State the blood parasite species.
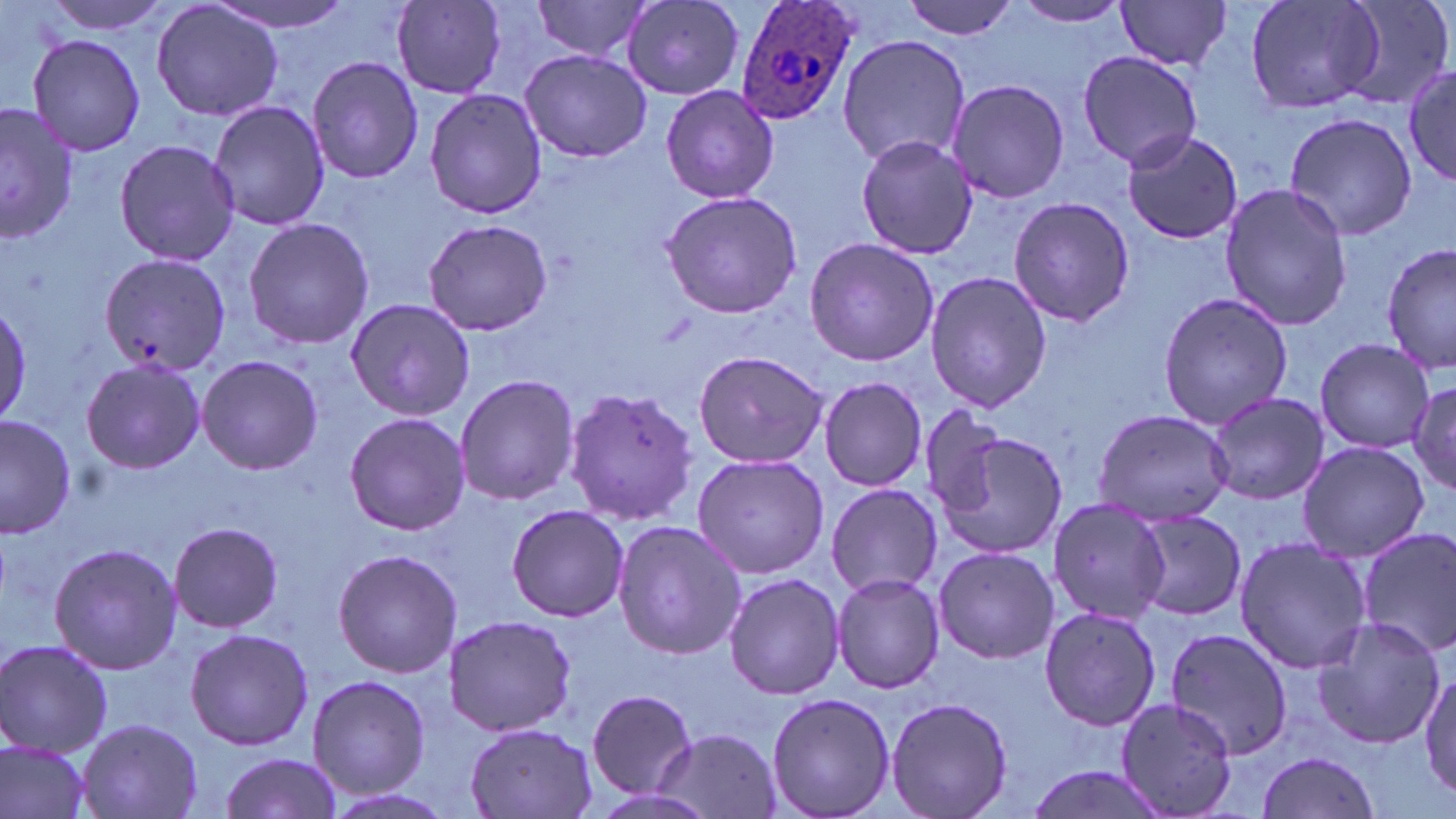
Plasmodium ovale.

image_size: 1456×819 pixels
modality: optical microscopy
magnification: 1000x
stain: May-Grünwald-Giemsa
field_of_view: one of a larger specimen
plasmodium_ovale_infected_red_blood_cell_locations: 'approximate bounding boxes as (x1, y1, x2, y2) in pixels: (732, 0, 860, 127)'
preparation: thin blood film
uninfected_red_blood_cell_locations: 'approximate bounding boxes as (x1, y1, x2, y2) in pixels: (40, 0, 174, 34), (205, 0, 357, 34), (900, 0, 1023, 40), (1012, 0, 1132, 28), (1113, 0, 1236, 72), (1245, 0, 1386, 116), (1344, 0, 1453, 111), (151, 1, 284, 123), (530, 1, 656, 62), (622, 1, 743, 102), (390, 2, 508, 97), (26, 32, 147, 157), (836, 33, 971, 169), (519, 49, 651, 163), (1076, 49, 1203, 170), (307, 56, 425, 185), (1403, 64, 1455, 191), (945, 78, 1069, 205), (659, 82, 779, 204), (423, 87, 547, 220), (208, 99, 331, 230), (1, 102, 77, 244), (1283, 112, 1419, 242), (1120, 129, 1243, 245), (854, 134, 979, 261), (113, 139, 239, 265), (1218, 183, 1354, 330), (659, 189, 807, 320), (1009, 197, 1136, 325), (242, 216, 373, 351), (421, 218, 555, 337), (803, 237, 940, 368), (1380, 242, 1455, 377), (98, 253, 229, 375), (924, 270, 1053, 412), (1157, 290, 1293, 432), (0, 297, 31, 425), (344, 297, 478, 423), (1315, 338, 1433, 454), (691, 348, 831, 467), (194, 354, 325, 475), (80, 357, 207, 475), (454, 374, 581, 506), (819, 376, 929, 491), (1405, 377, 1456, 496), (562, 386, 701, 524), (1204, 391, 1330, 506), (1093, 407, 1235, 526), (0, 413, 78, 539), (344, 413, 471, 536), (931, 421, 1069, 562), (1297, 441, 1430, 562), (690, 455, 832, 580), (827, 482, 944, 599), (1046, 498, 1174, 624), (504, 503, 632, 622), (1130, 507, 1247, 623), (612, 520, 744, 661), (168, 521, 284, 634), (1357, 527, 1456, 657), (1235, 537, 1370, 673), (49, 542, 185, 676), (931, 547, 1062, 664), (334, 548, 461, 679), (723, 572, 845, 701), (832, 572, 946, 694), (1039, 604, 1165, 731), (442, 613, 581, 737), (1309, 613, 1446, 751), (184, 627, 314, 751), (1165, 627, 1294, 758), (0, 638, 113, 756), (1420, 668, 1455, 806), (306, 674, 431, 797), (586, 688, 695, 800), (765, 690, 895, 819), (884, 696, 1014, 819), (1114, 697, 1242, 819), (76, 716, 202, 819), (462, 722, 602, 817), (655, 728, 782, 818), (1, 737, 94, 819), (1255, 749, 1385, 819), (215, 751, 343, 819), (1023, 760, 1173, 819), (319, 788, 464, 819)'